Assess this cell for malaria.
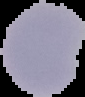

It is uninfected.

Cell region segmented out of the field of view; the surrounding area is masked to black. From a thin blood film. Image is 85×97 pixels.